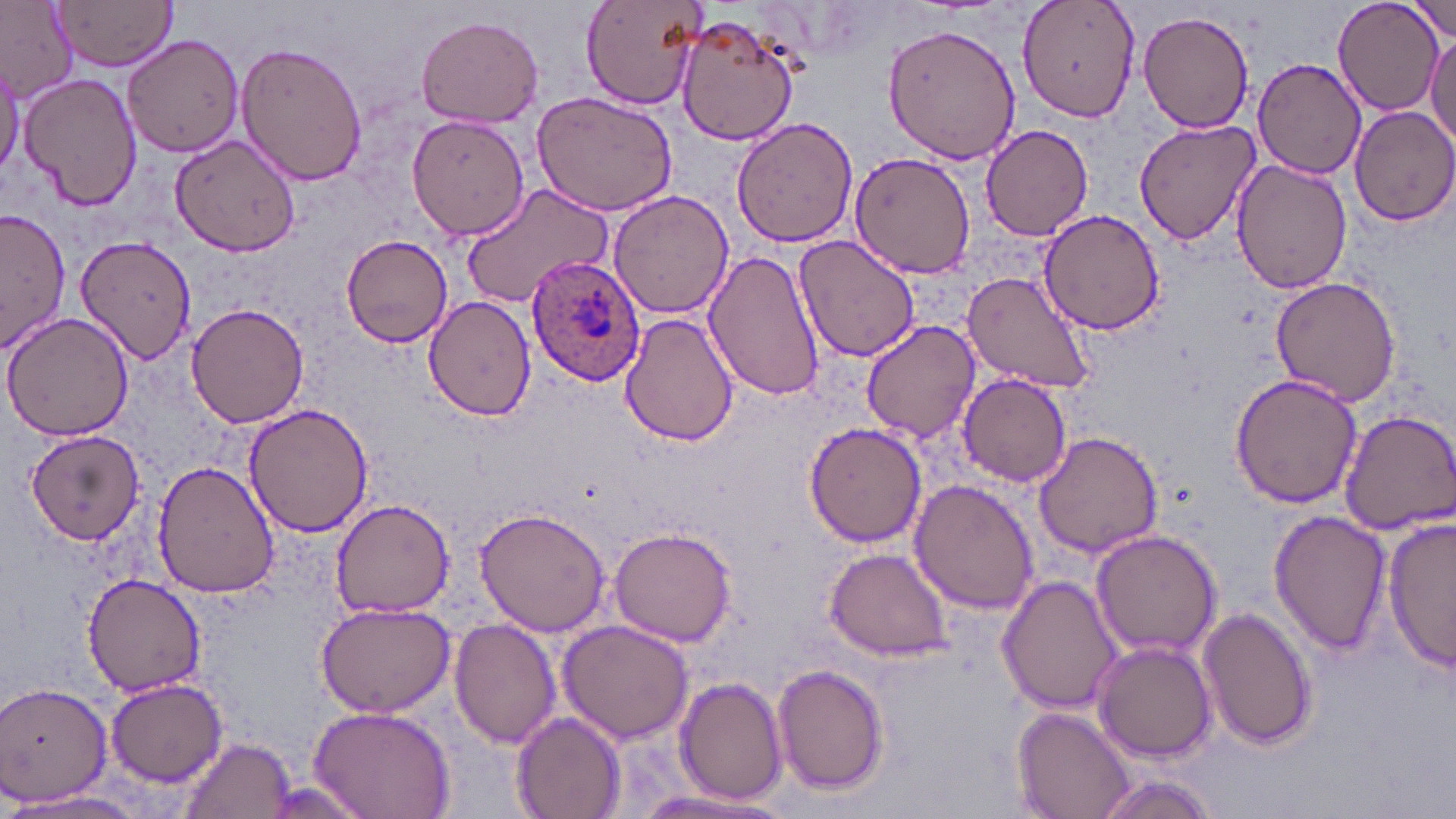 Approximate bounding boxes as (x1,y1)-(x2,y2) corner pairs in pixels. Uninfected red blood cell locations: (0,0)-(79,103), (55,0)-(180,70), (1016,0)-(1142,122), (1410,0)-(1454,42), (579,1)-(708,111), (1334,1)-(1441,116), (1138,10)-(1255,133), (673,11)-(801,145), (416,14)-(544,127), (883,20)-(1022,164), (122,32)-(245,159), (1426,34)-(1456,150), (234,39)-(368,187), (1252,57)-(1368,180), (0,65)-(24,181), (20,72)-(142,211), (531,90)-(679,215), (1348,104)-(1456,226), (406,115)-(530,241), (730,116)-(861,249), (1133,120)-(1261,246), (981,124)-(1096,242), (171,137)-(299,259), (849,150)-(976,278), (1231,159)-(1352,295), (462,183)-(615,308), (606,189)-(732,322), (2,207)-(70,354), (1036,209)-(1168,337), (76,234)-(196,366), (339,234)-(453,349), (792,235)-(921,362), (704,248)-(825,403), (960,271)-(1099,395), (1270,276)-(1402,406), (423,298)-(536,422), (186,301)-(309,427), (0,311)-(136,442), (621,313)-(739,447), (861,319)-(981,443), (958,373)-(1072,486), (1231,374)-(1363,508), (244,403)-(374,538), (1337,408)-(1456,535), (803,421)-(925,548), (24,429)-(145,546), (1033,430)-(1164,558), (152,459)-(278,598), (909,479)-(1042,615), (330,497)-(456,619), (476,508)-(610,637), (1271,510)-(1391,654), (1384,515)-(1456,675), (609,527)-(737,646), (1090,532)-(1223,660), (824,547)-(953,659), (80,574)-(206,697), (997,575)-(1124,715), (314,600)-(455,717), (1198,605)-(1318,751), (450,618)-(561,749), (558,619)-(695,744), (1094,641)-(1216,764), (772,662)-(888,793), (676,676)-(790,805), (107,679)-(228,786), (0,680)-(115,807), (306,706)-(454,819), (1013,707)-(1135,819), (512,710)-(628,818), (177,736)-(294,819), (1089,773)-(1220,817), (628,790)-(782,817), (9,791)-(151,817). Plasmodium ovale-infected red blood cell locations: (527,255)-(647,389). Slide-level diagnosis: Plasmodium ovale. May-Grünwald-Giemsa stain. Image is 1456×819 pixels. Thin blood smear. 1000x magnification. Light microscopy. One field of a larger specimen.